Comment on the morphology of the red blood cells.
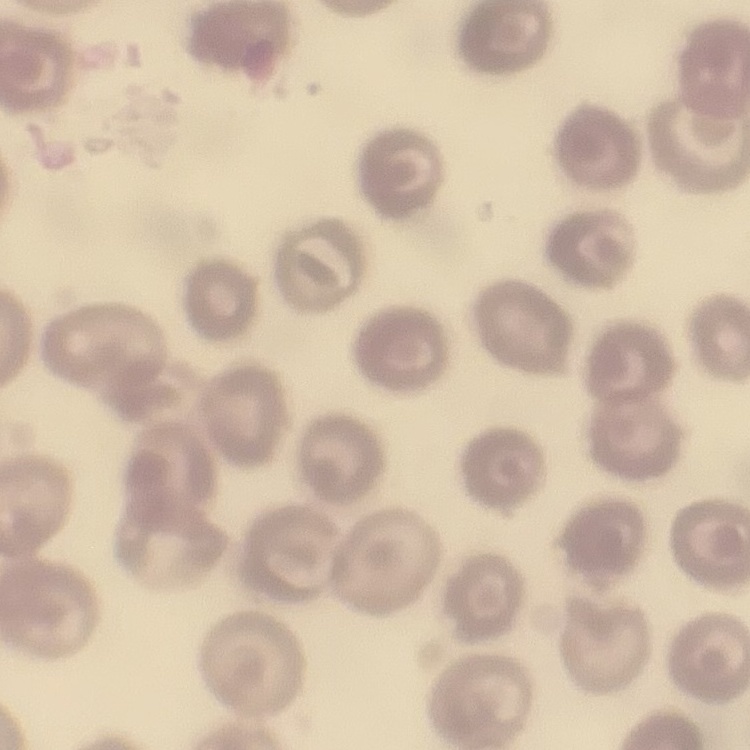
They show no rouleaux formation.

Thin peripheral smear. Field's or Giemsa stain. Square crop of a larger photomicrograph.